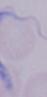

modality = photomicrograph
identification = trypanosome
magnification = 1000x